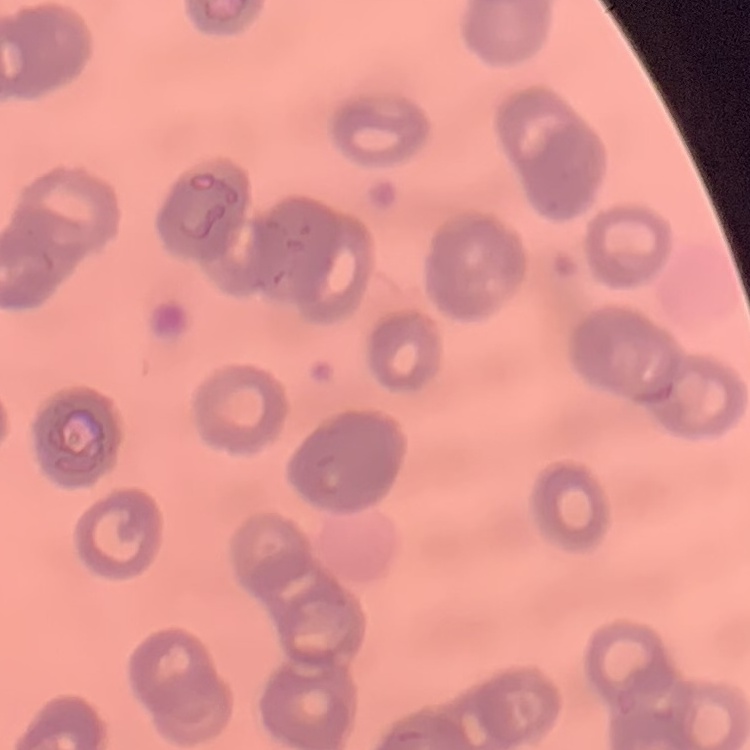
Summary:
  - Erythrocyte morphology: rouleaux formation
  - Stain: Field's or Giemsa
  - Preparation: thin peripheral smear
  - Image type: one tile cut from a larger photomicrograph